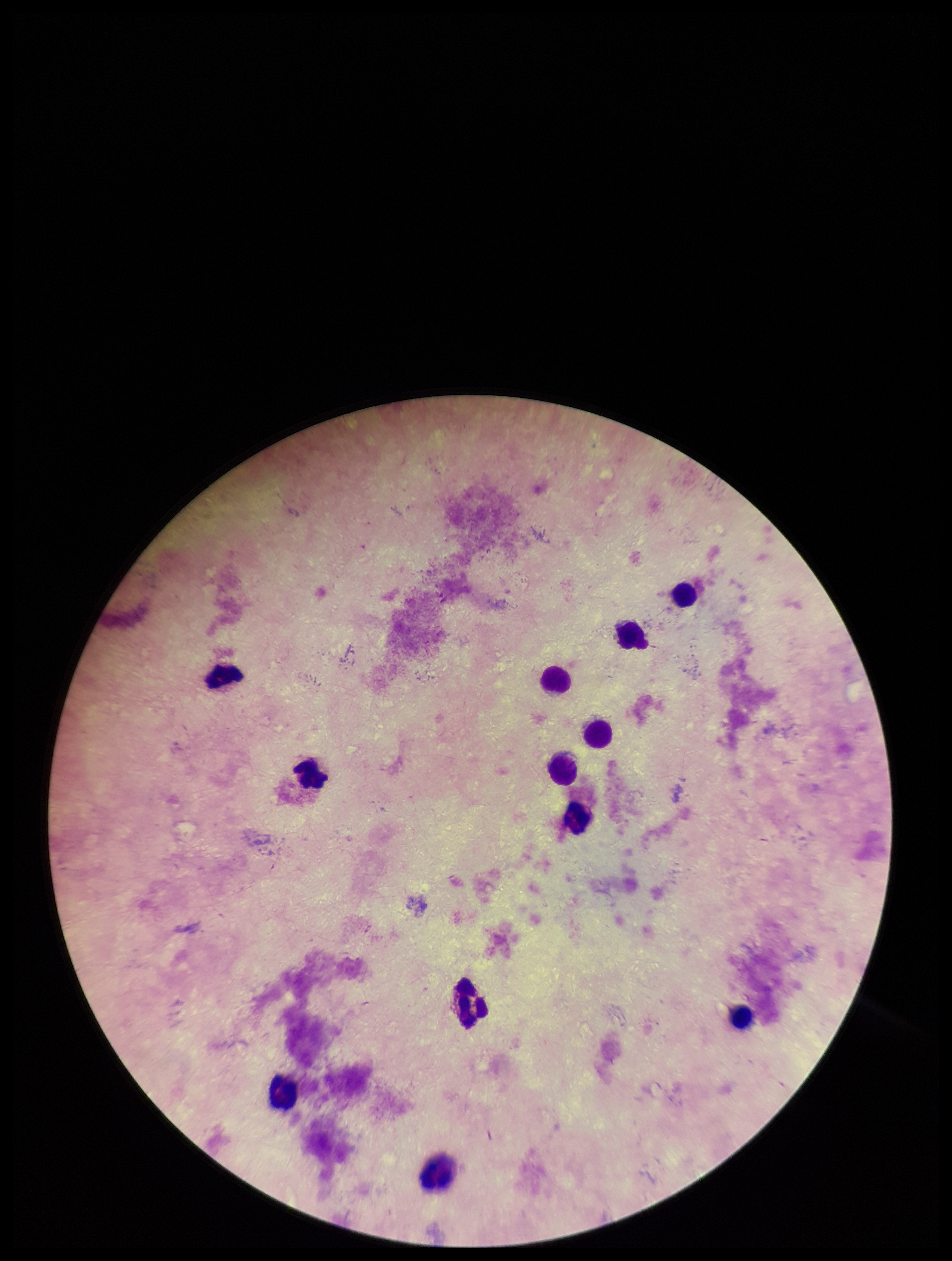

Parasite count: 0. Photographed through the microscope eyepiece with a smartphone camera. Leukocyte count: 12. Plasmodium parasites: none identified. Preparation: thick smear. Stained with Giemsa. Image is 952×1261 pixels. Patient malaria status: negative. Single field of view.